Classify this cell by malaria status.
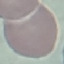

It is uninfected.

Automatically extracted cell patch, resized to 64 × 64 pixels. Giemsa stain. Thin smear of blood. Acquired by smartphone through the microscope eyepiece.